Name the cell type shown.
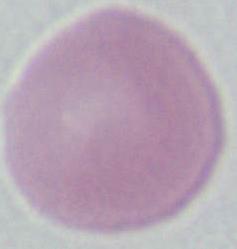
This is an erythrocyte.

magnification = 1000x
modality = micrograph